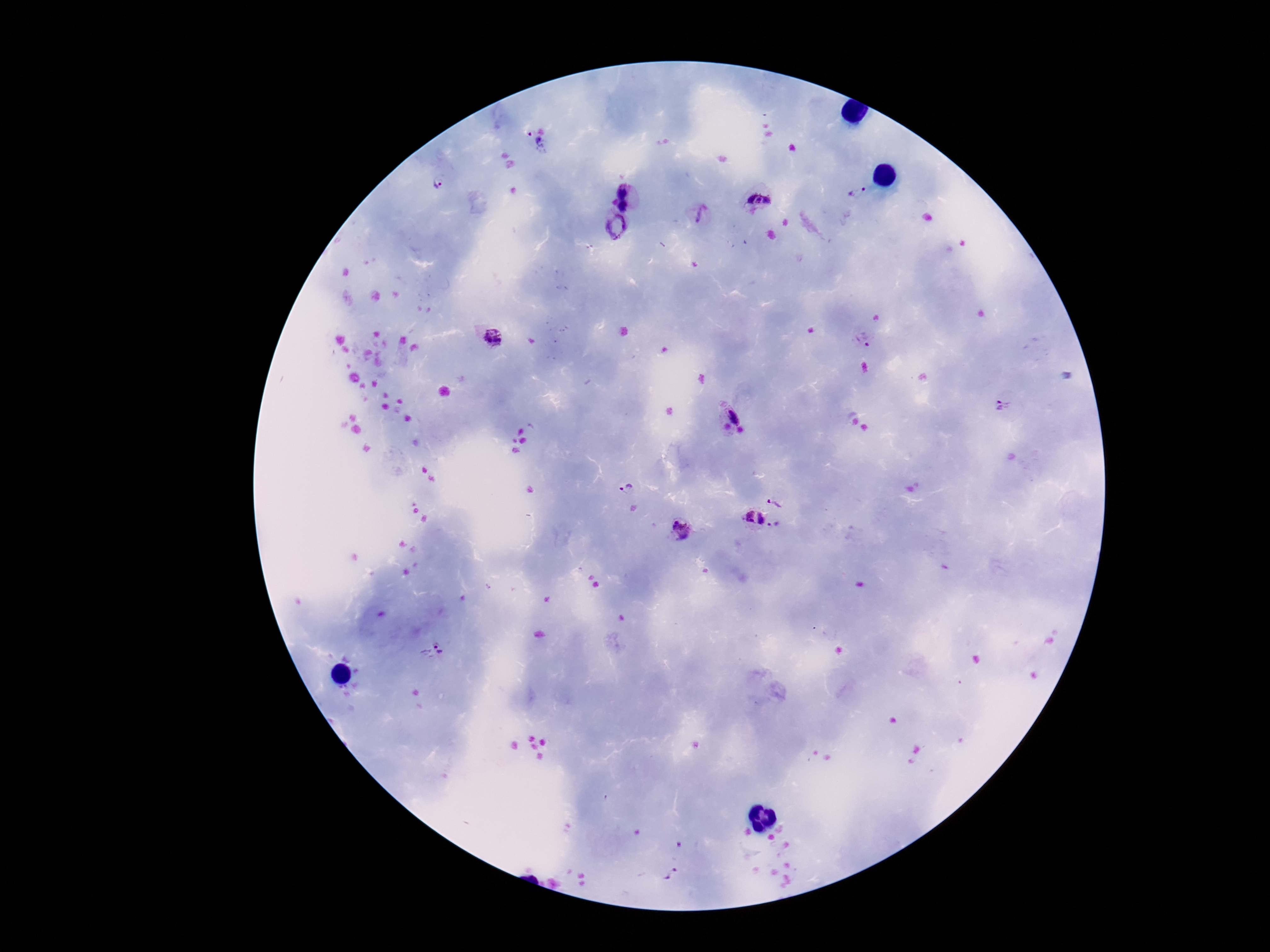
Approximate centers as {x, y} in pixels. Plasmodium parasite locations: {532, 145}, {440, 182}, {859, 192}, {627, 195}, {759, 196}, {699, 217}, {615, 227}, {490, 336}, {863, 340}, {1003, 407}, {732, 422}, {628, 489}, {778, 500}, {754, 518}, {776, 528}, {681, 529}, {434, 651}. Smartphone photograph taken through the microscope eyepiece. Patient malaria status: positive. Giemsa-stained preparation. 100x magnification. Image is 1270×952 pixels. Single field of view. Thick blood smear.